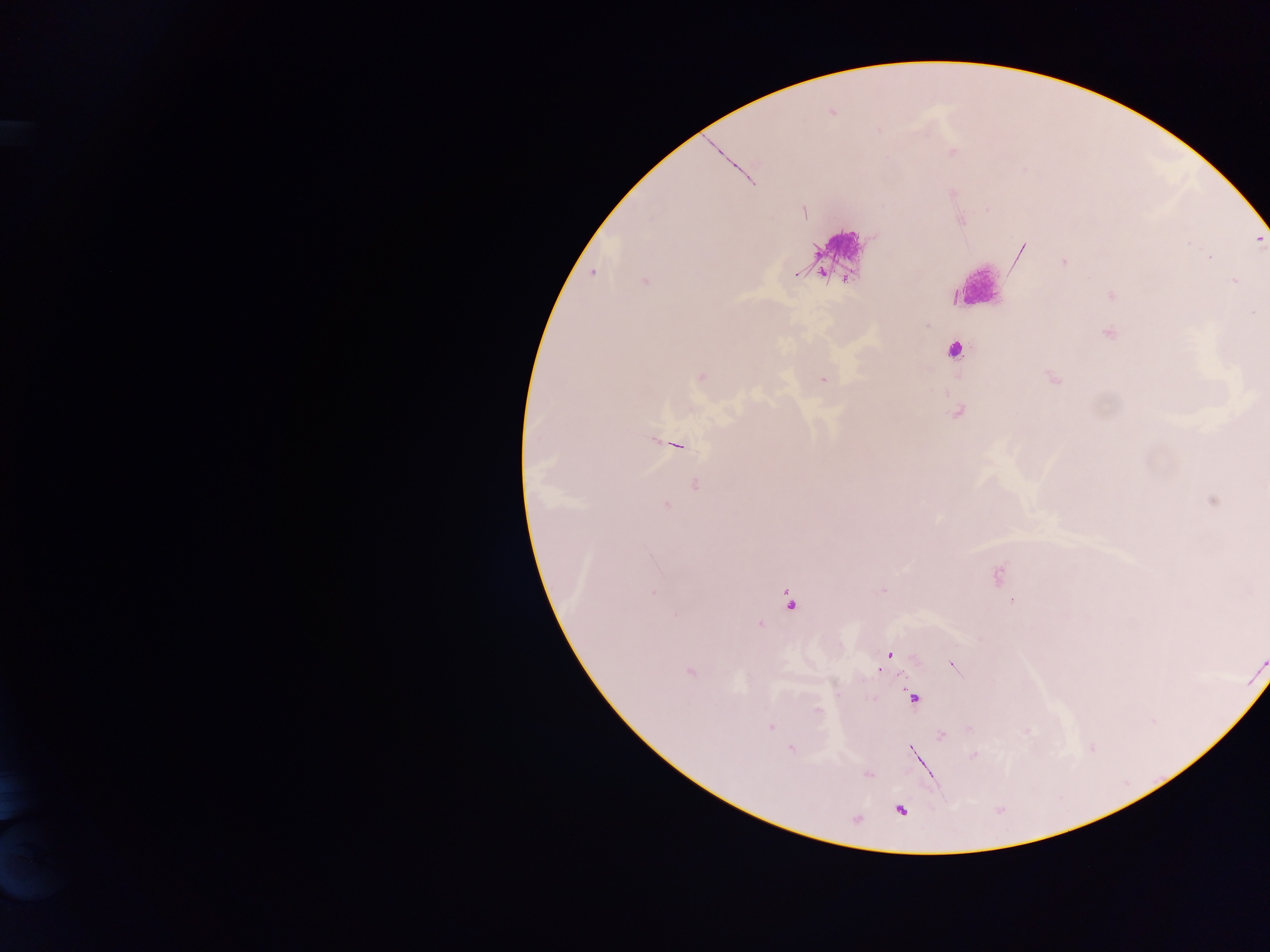
preparation = thick blood smear
capture = mobile-phone photograph through a microscope
country = Ghana
leukocyte locations = approximate centers as {x, y} in pixels: {839, 254}, {974, 287}, {952, 350}
Plasmodium parasite locations = approximate centers as {x, y} in pixels: {831, 112}, {716, 148}, {1019, 253}, {1064, 262}, {592, 273}, {796, 274}, {1234, 280}, {645, 281}, {1110, 295}, {1107, 333}, {701, 376}, {1052, 378}, {822, 379}, {957, 412}, {676, 444}, {694, 484}, {1212, 500}, {665, 505}, {997, 576}, {883, 590}, {789, 602}, {758, 625}, {888, 654}, {951, 663}, {878, 667}, {689, 671}, {912, 698}, {770, 726}, {941, 735}, {790, 749}, {912, 750}, {915, 750}, {973, 755}, {918, 760}, {868, 773}, {900, 809}
image size = 1270×952 pixels
field of view = single